Point out each Plasmodium parasite.
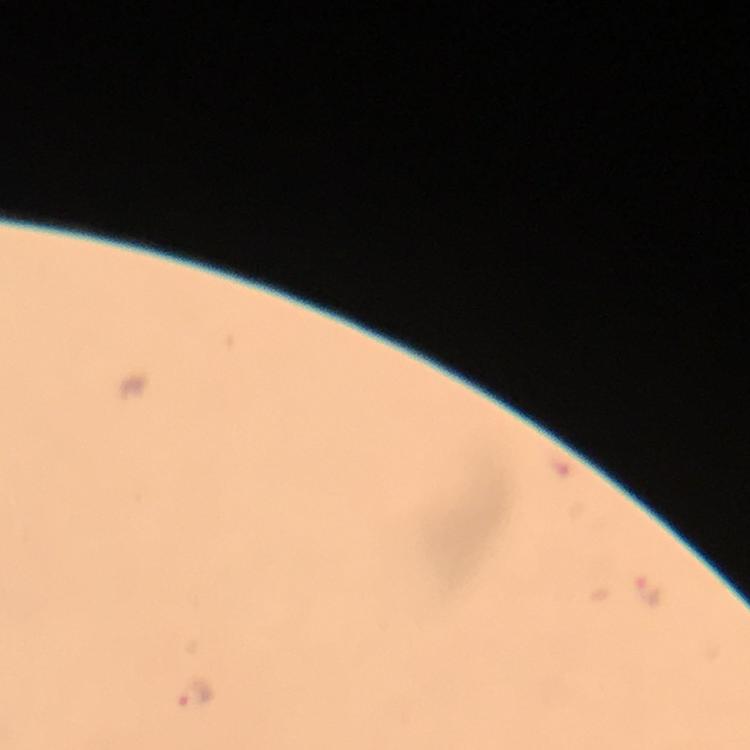

Approximate object centers, in pixels from the top-left corner.
Plasmodium parasites: (x=649, y=592), (x=194, y=697).

Summary:
  - Capture: smartphone camera through the microscope
  - Stain: Giemsa
  - Context: from a diagnostic examination for malaria
  - Cropped from: one field of view
  - Image size: 750×750 pixels
  - Immersion oil: applied
  - Magnification: 100x
  - Preparation: thick blood film